Describe the morphology of the red blood cells.
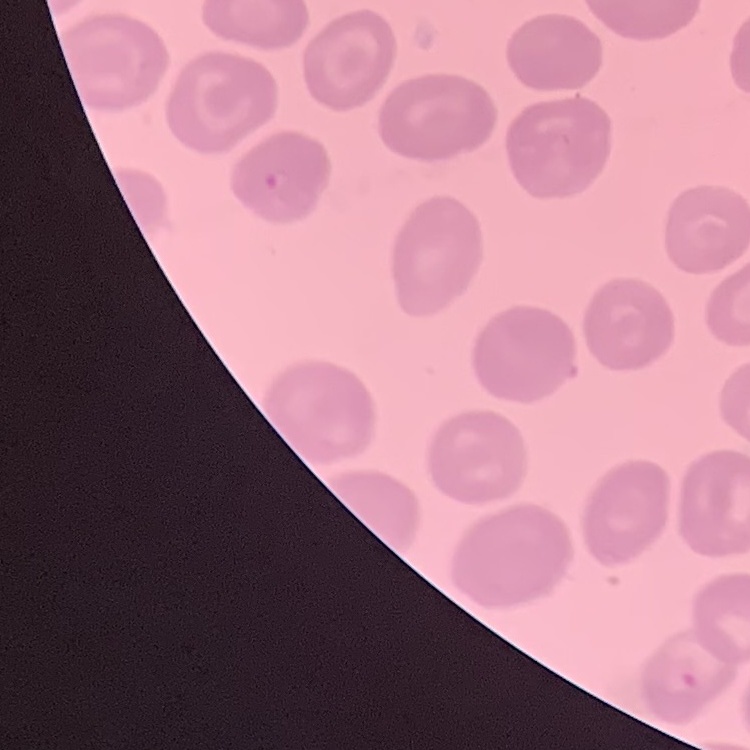

No rouleaux formation.

Thin peripheral smear. One tile cut from a larger photomicrograph. Stained with either Field's or Giemsa.